Point out each malaria parasite.
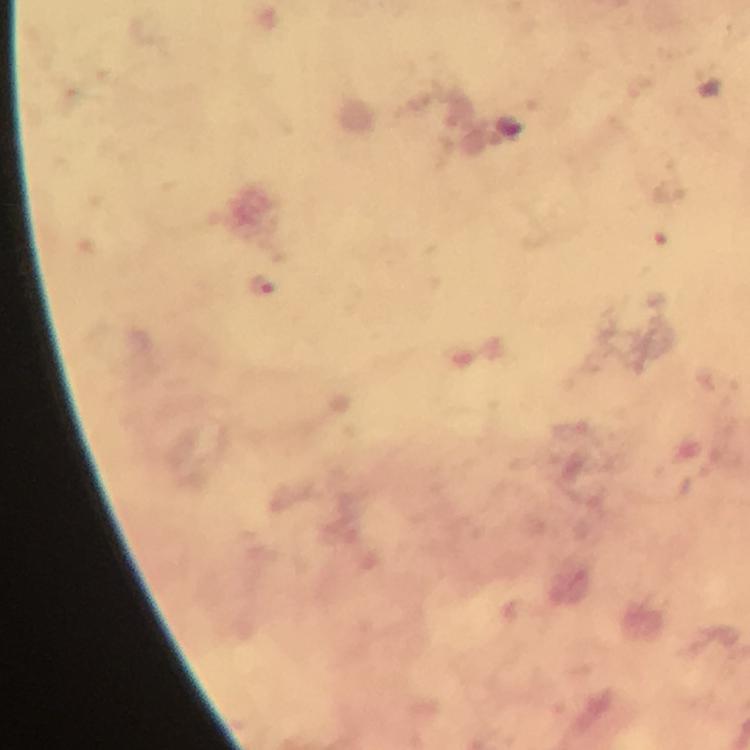

Approximate centers as (x, y) in pixels.
Malaria parasites: (261, 285).

Photographed through the microscope with a smartphone camera. From a diagnostic examination for malaria. Thick smear. Giemsa-stained preparation. Immersion oil was used. Image is 750×750 pixels. At 100x magnification. Cropped region of a single field of view.